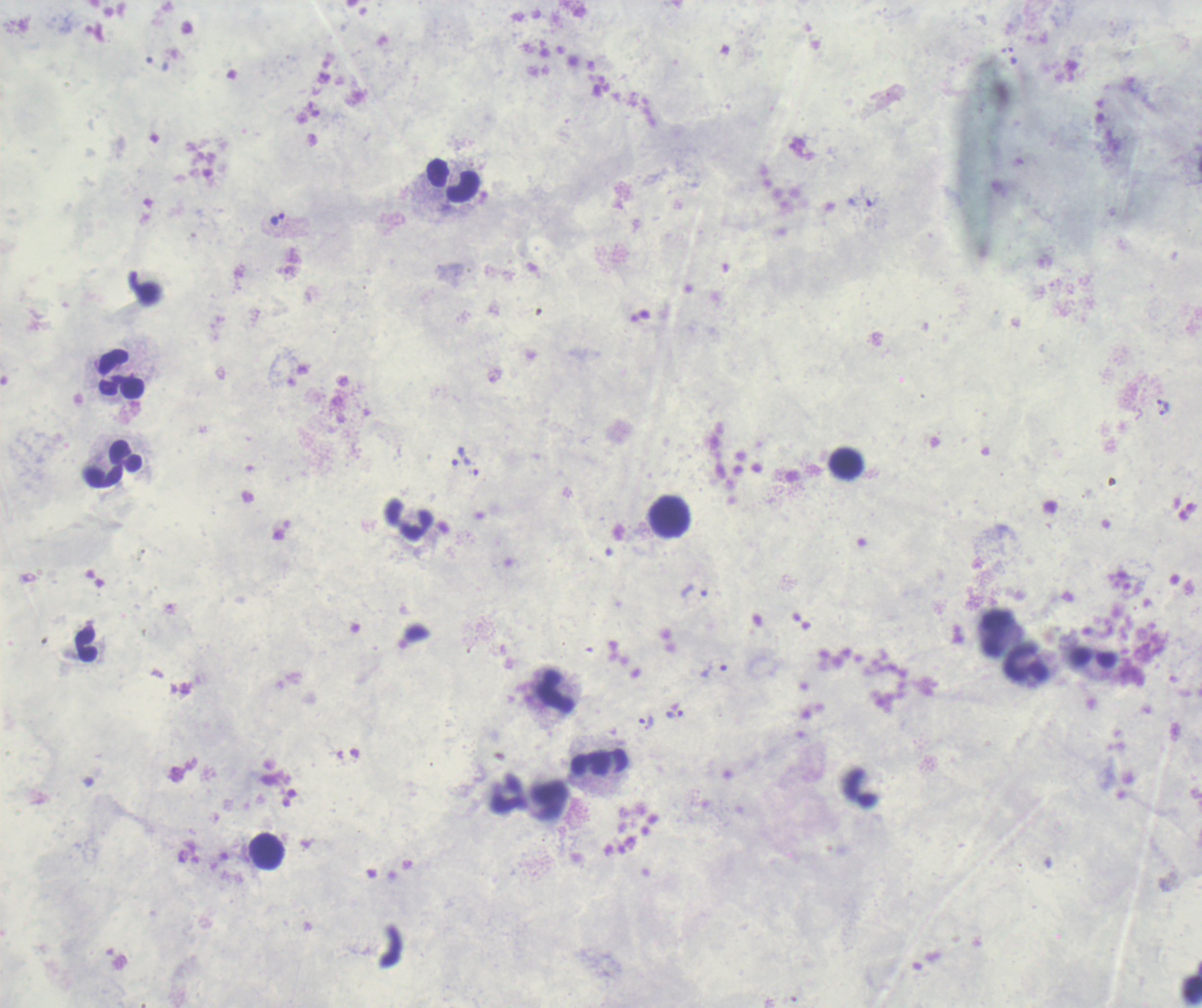 Approximate object centers, in pixels from the top-left corner. Leukocyte locations: (x=454, y=181), (x=123, y=374), (x=114, y=464), (x=671, y=517), (x=410, y=522), (x=996, y=633), (x=87, y=645), (x=1028, y=663), (x=555, y=692), (x=600, y=764), (x=268, y=851). Trophozoite locations: (x=1012, y=56), (x=861, y=202), (x=277, y=220), (x=1161, y=403), (x=1163, y=411), (x=460, y=456), (x=694, y=590), (x=714, y=668), (x=674, y=715), (x=646, y=723). Captured at 100x magnification. Background quality: poor. Image is 1202×1008 pixels. Thick blood film. Romanowsky-stained preparation. Previously used in a real diagnosis. Single field of view. Result: Plasmodium parasites detected.